Report the malaria status of this cell.
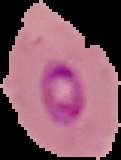
It is parasitized.

Summary:
  - Image type: segmented cell region with the area outside set to black
  - Preparation: thin blood film
  - Image size: 121×160 pixels